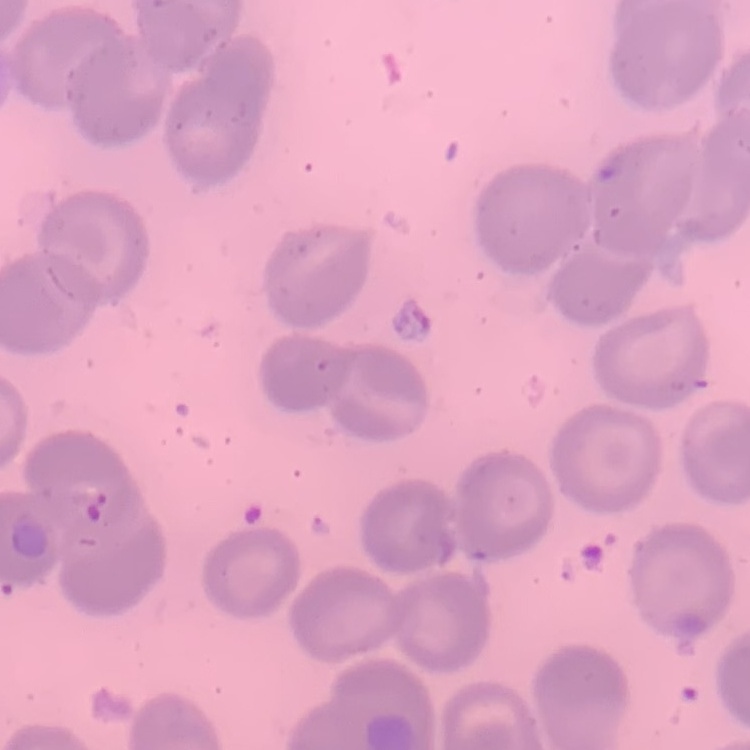
The erythrocytes exhibit no rouleaux formation. One tile cut from a larger photomicrograph. Thin blood smear. Field's or Giemsa stain.